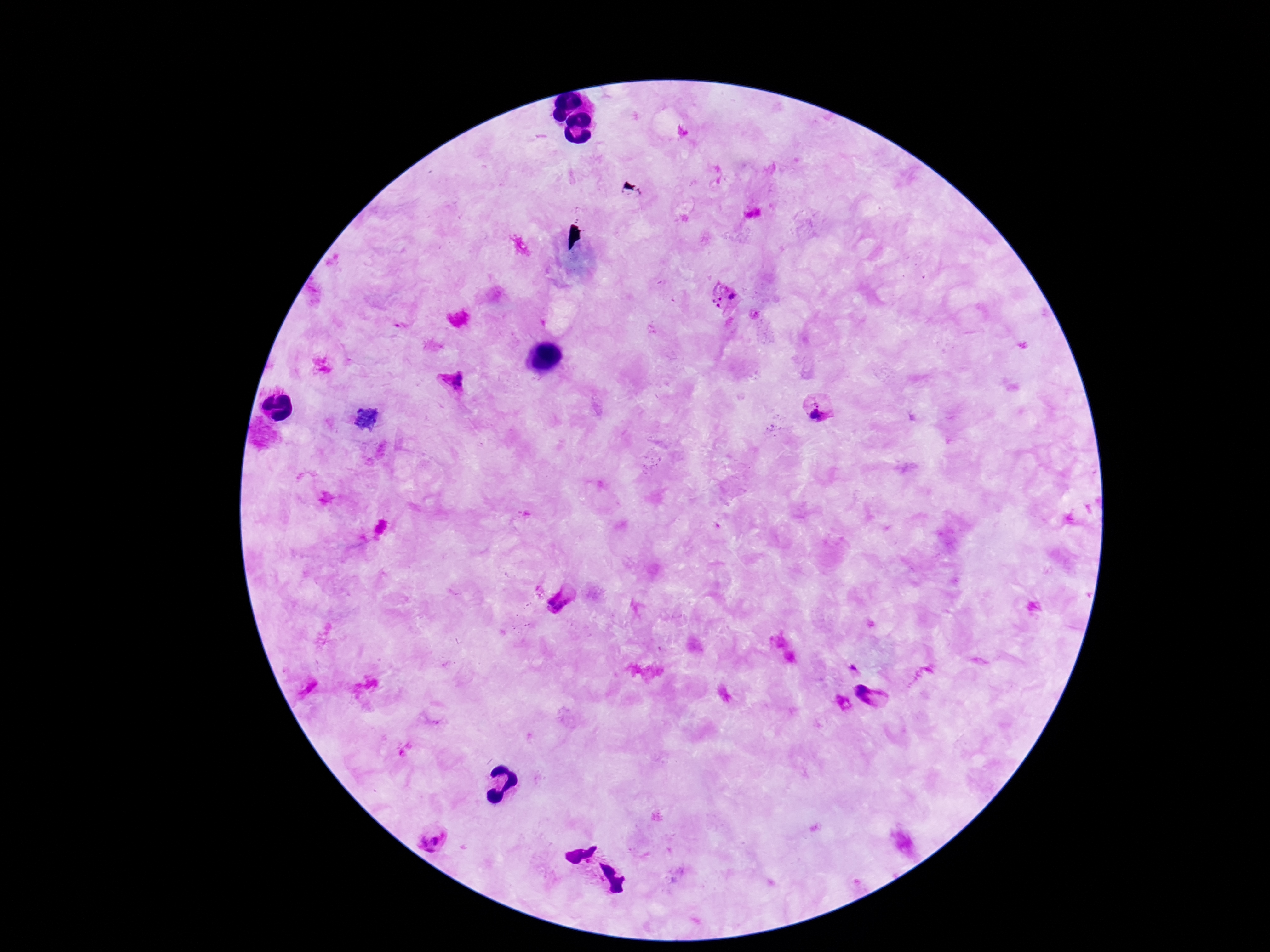
Approximate centers as [x, y] in pixels. Plasmodium parasite locations: [724, 288], [732, 296], [720, 299], [713, 302], [718, 305], [755, 314], [452, 382], [817, 402], [818, 418], [561, 603], [869, 695], [432, 839]. Image is 1270×952 pixels. One field from this slide. 100x magnification. Patient malaria status: positive. Thick blood smear. Smartphone photograph taken through the microscope eyepiece. Giemsa-stained preparation.